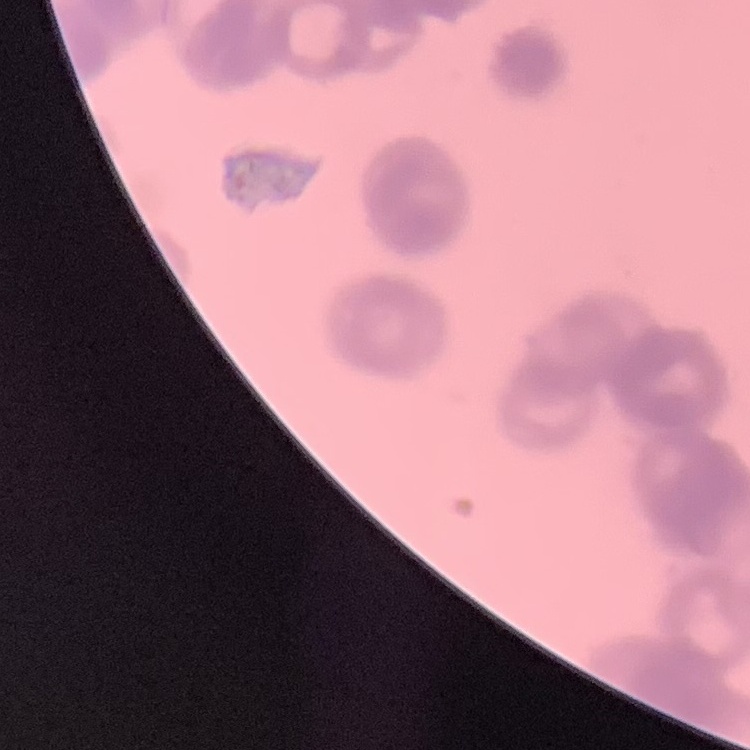
erythrocyte morphology = rouleaux formation
preparation = thin peripheral smear
image type = square crop of a larger photomicrograph
stain = Field's or Giemsa